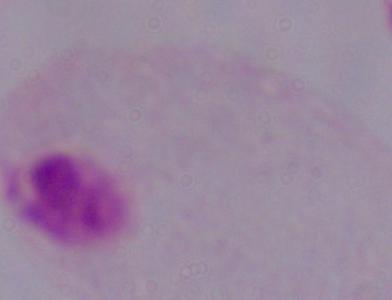
{
  "magnification": "1000x",
  "modality": "photomicrograph",
  "identification": "trichomonad"
}